Report the malaria status of this cell.
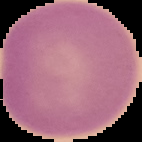

Uninfected.

Summary:
  - Preparation: thin blood smear
  - Image type: segmented cell region with the area outside set to black
  - Image size: 142×142 pixels